Give the position of every malaria parasite.
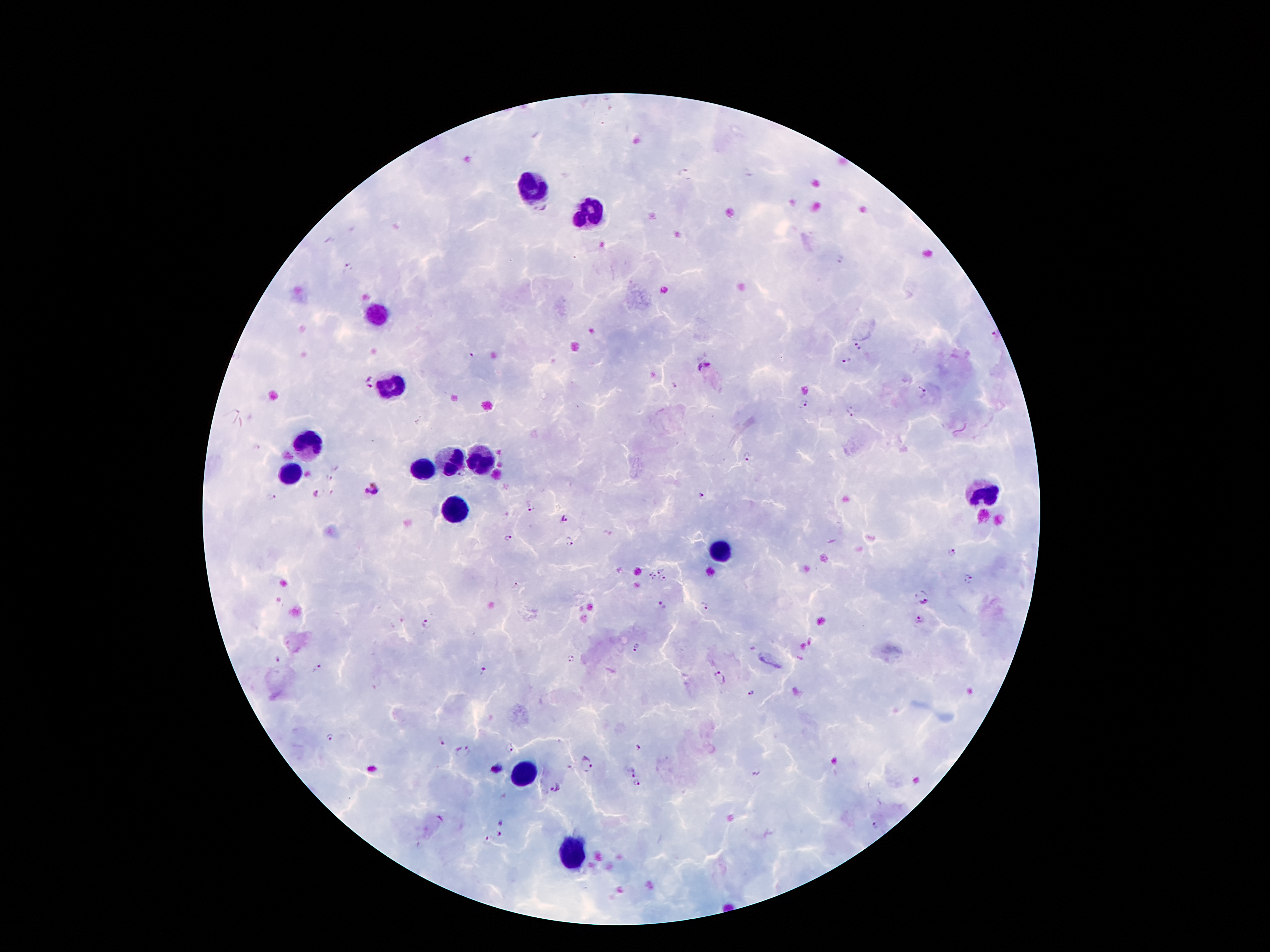

Approximate centers as {x, y} in pixels.
Malaria parasites: {685, 172}, {543, 209}, {841, 261}, {349, 267}, {995, 335}, {858, 348}, {472, 356}, {845, 361}, {703, 367}, {369, 383}, {675, 386}, {923, 393}, {803, 405}, {850, 414}, {743, 457}, {463, 475}, {328, 477}, {373, 490}, {315, 493}, {700, 495}, {270, 497}, {531, 507}, {565, 518}, {508, 539}, {569, 541}, {953, 553}, {661, 568}, {650, 573}, {654, 577}, {663, 579}, {967, 579}, {516, 586}, {924, 598}, {706, 606}, {663, 607}, {919, 621}, {426, 624}, {638, 647}, {571, 658}, {279, 660}, {317, 668}, {482, 671}, {720, 678}, {750, 693}, {330, 737}, {442, 742}, {508, 748}, {640, 749}, {462, 752}, {588, 765}, {497, 768}, {631, 770}, {756, 774}, {638, 785}, {556, 787}, {502, 823}, {876, 825}, {499, 834}, {487, 842}.

Leukocyte locations: {533, 186}, {592, 209}, {375, 317}, {393, 385}, {310, 445}, {478, 461}, {445, 466}, {424, 472}, {291, 477}, {979, 497}, {454, 512}, {722, 553}, {522, 778}, {574, 851}. Photographed through the microscope eyepiece with a smartphone camera. Giemsa stain. Patient malaria status: infected with Plasmodium falciparum. Thick blood smear. Image is 1270×952 pixels. 100x magnification. Single field of view.